Describe the morphology of the erythrocytes.
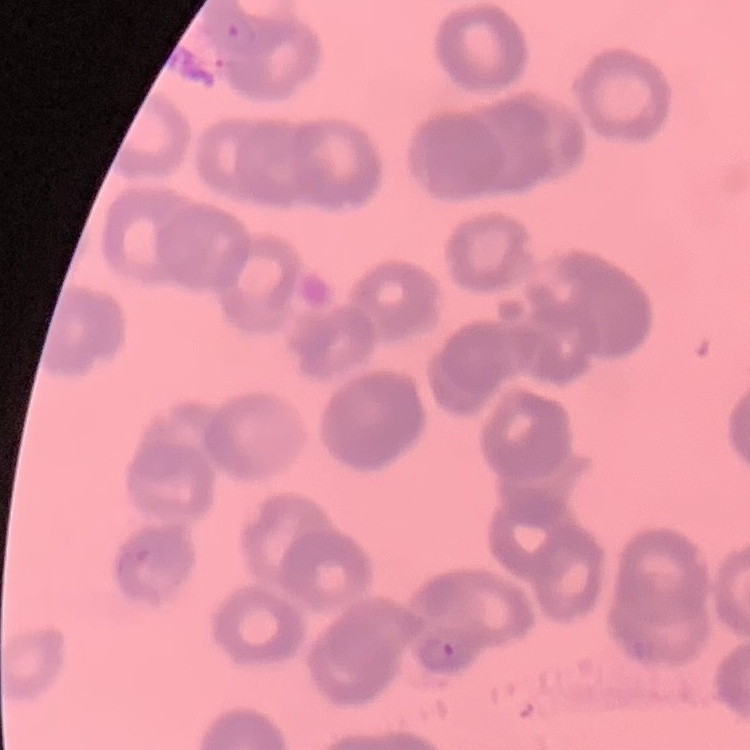

Rouleaux formation.

preparation = thin blood smear
stain = Field's or Giemsa
image type = one tile cut from a larger photomicrograph